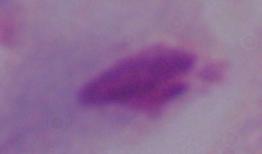

modality = photomicrograph
magnification = 1000x
identification = trichomonad